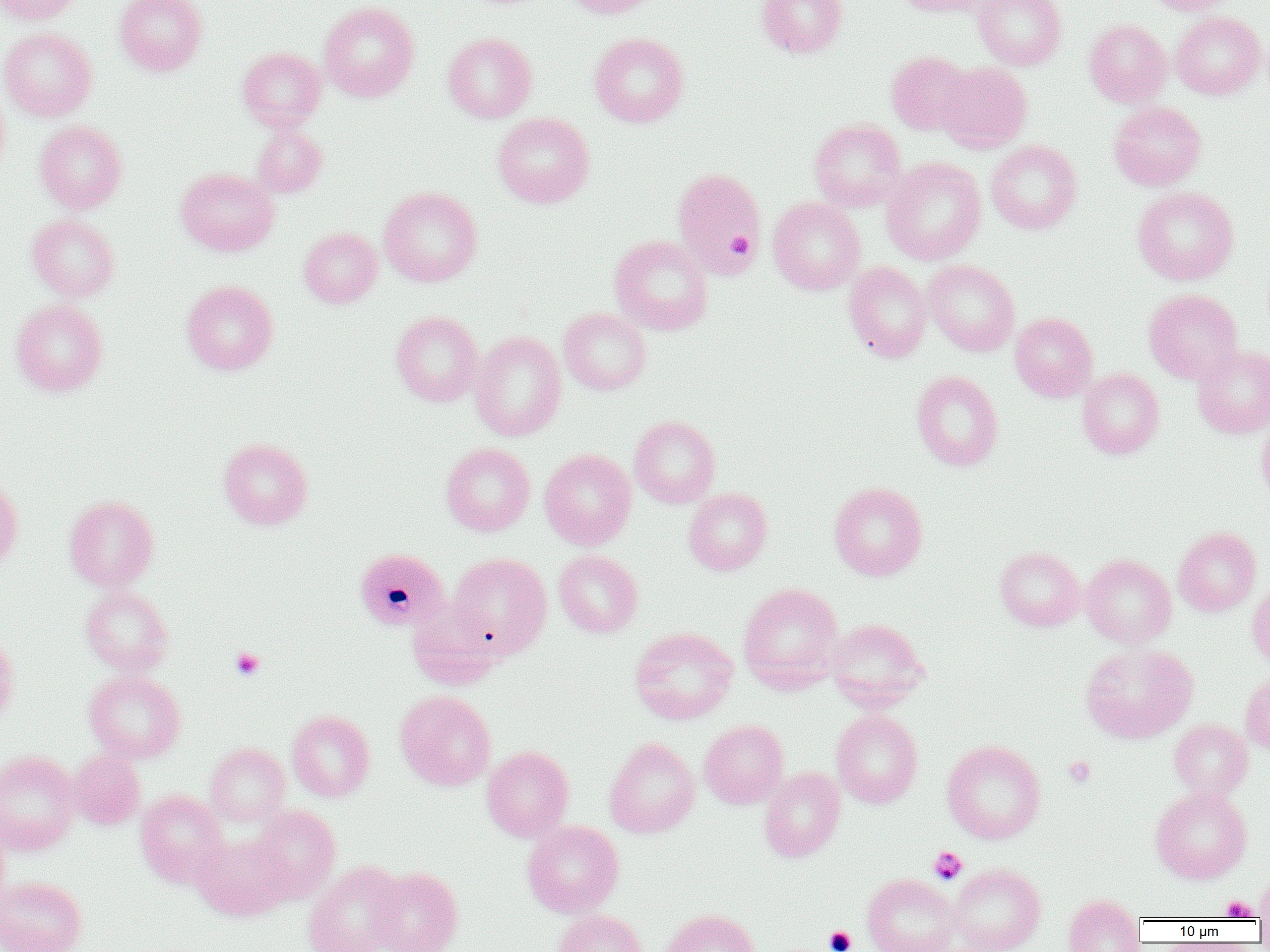

Approximate bounding boxes as named x1/y1/x2/y2 corners in pixels. Platelet locations: (x1=727, y1=232, x2=755, y2=256), (x1=230, y1=648, x2=265, y2=680), (x1=1064, y1=757, x2=1096, y2=787), (x1=928, y1=846, x2=968, y2=884), (x1=1221, y1=895, x2=1257, y2=920), (x1=824, y1=925, x2=857, y2=952). Uninfected red blood cell locations: (x1=0, y1=0, x2=80, y2=24), (x1=115, y1=0, x2=207, y2=76), (x1=562, y1=0, x2=660, y2=18), (x1=756, y1=0, x2=848, y2=58), (x1=893, y1=0, x2=992, y2=16), (x1=973, y1=0, x2=1067, y2=70), (x1=1142, y1=0, x2=1235, y2=15), (x1=318, y1=1, x2=419, y2=102), (x1=1170, y1=11, x2=1266, y2=99), (x1=1084, y1=19, x2=1171, y2=107), (x1=0, y1=27, x2=97, y2=121), (x1=443, y1=32, x2=537, y2=123), (x1=589, y1=32, x2=689, y2=127), (x1=237, y1=47, x2=326, y2=131), (x1=886, y1=51, x2=975, y2=135), (x1=936, y1=62, x2=1032, y2=153), (x1=0, y1=87, x2=10, y2=181), (x1=1108, y1=101, x2=1206, y2=191), (x1=493, y1=112, x2=594, y2=208), (x1=809, y1=118, x2=906, y2=212), (x1=35, y1=120, x2=127, y2=214), (x1=251, y1=123, x2=327, y2=198), (x1=986, y1=140, x2=1082, y2=234), (x1=882, y1=157, x2=986, y2=266), (x1=176, y1=167, x2=279, y2=256), (x1=672, y1=167, x2=766, y2=280), (x1=379, y1=187, x2=482, y2=287), (x1=1133, y1=187, x2=1238, y2=285), (x1=768, y1=197, x2=865, y2=295), (x1=26, y1=213, x2=120, y2=301), (x1=299, y1=227, x2=382, y2=308), (x1=609, y1=235, x2=713, y2=335), (x1=923, y1=260, x2=1020, y2=356), (x1=844, y1=261, x2=932, y2=363), (x1=181, y1=280, x2=278, y2=375), (x1=1144, y1=289, x2=1243, y2=384), (x1=10, y1=299, x2=108, y2=396), (x1=558, y1=308, x2=652, y2=395), (x1=391, y1=311, x2=484, y2=406), (x1=1010, y1=312, x2=1098, y2=401), (x1=469, y1=332, x2=566, y2=441), (x1=1192, y1=345, x2=1270, y2=438), (x1=1077, y1=368, x2=1164, y2=459), (x1=911, y1=370, x2=1003, y2=471), (x1=1257, y1=415, x2=1270, y2=510), (x1=629, y1=416, x2=721, y2=508), (x1=218, y1=438, x2=313, y2=529), (x1=440, y1=442, x2=535, y2=536), (x1=539, y1=448, x2=636, y2=550), (x1=0, y1=477, x2=23, y2=571), (x1=829, y1=482, x2=928, y2=581), (x1=683, y1=488, x2=772, y2=575), (x1=63, y1=495, x2=159, y2=591), (x1=1173, y1=527, x2=1261, y2=616), (x1=995, y1=547, x2=1085, y2=631), (x1=553, y1=550, x2=643, y2=637), (x1=449, y1=553, x2=551, y2=657), (x1=1080, y1=554, x2=1176, y2=648), (x1=1247, y1=580, x2=1270, y2=669), (x1=738, y1=583, x2=844, y2=693), (x1=80, y1=585, x2=174, y2=677), (x1=407, y1=598, x2=503, y2=690), (x1=826, y1=618, x2=930, y2=711), (x1=630, y1=627, x2=738, y2=724), (x1=0, y1=633, x2=19, y2=728), (x1=1080, y1=642, x2=1198, y2=743), (x1=85, y1=671, x2=186, y2=763), (x1=1241, y1=671, x2=1270, y2=756), (x1=395, y1=690, x2=497, y2=791), (x1=287, y1=710, x2=375, y2=802), (x1=831, y1=710, x2=923, y2=808), (x1=699, y1=720, x2=788, y2=809), (x1=1169, y1=720, x2=1252, y2=799), (x1=604, y1=737, x2=700, y2=838), (x1=941, y1=740, x2=1046, y2=844), (x1=205, y1=743, x2=290, y2=826), (x1=481, y1=746, x2=574, y2=842), (x1=69, y1=749, x2=146, y2=830), (x1=0, y1=750, x2=80, y2=855), (x1=759, y1=767, x2=845, y2=862), (x1=1150, y1=786, x2=1252, y2=884), (x1=135, y1=790, x2=229, y2=887), (x1=250, y1=805, x2=341, y2=901), (x1=0, y1=820, x2=10, y2=911), (x1=522, y1=820, x2=624, y2=917), (x1=192, y1=833, x2=291, y2=920), (x1=303, y1=861, x2=406, y2=952), (x1=947, y1=863, x2=1045, y2=952), (x1=369, y1=867, x2=463, y2=952), (x1=1255, y1=870, x2=1270, y2=924), (x1=862, y1=873, x2=960, y2=952), (x1=0, y1=876, x2=86, y2=952), (x1=1063, y1=893, x2=1145, y2=952), (x1=554, y1=909, x2=648, y2=952), (x1=662, y1=909, x2=761, y2=952). Plasmodium malariae-infected red blood cell locations: (x1=354, y1=548, x2=449, y2=632). Slide-level diagnosis: Plasmodium malariae. One field of a larger specimen. Thin blood film. Image is 1270×952 pixels. Optical microscopy. Captured at 1000x magnification.